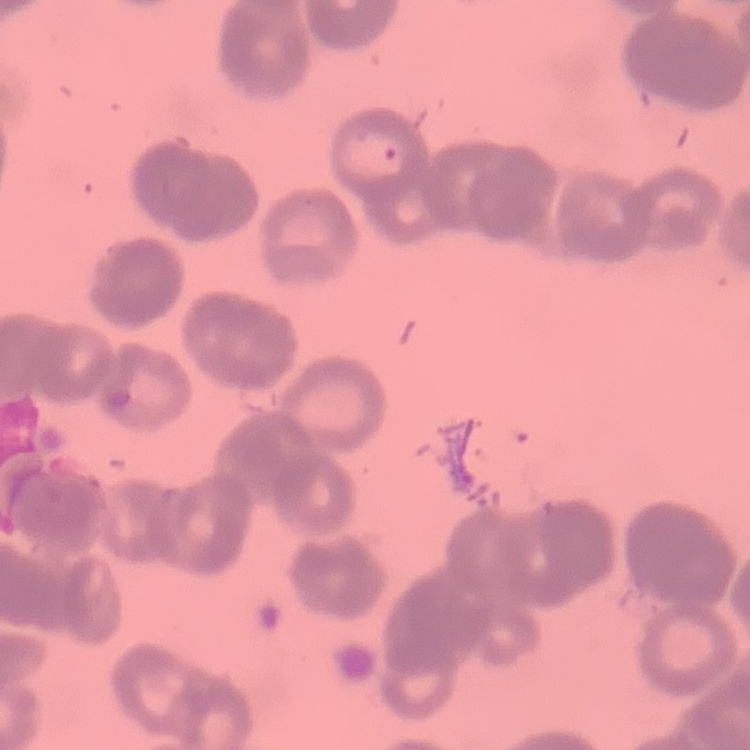 The erythrocytes exhibit rouleaux formation. Square crop of a larger photomicrograph. Stained with either Field's or Giemsa. Thin blood film.